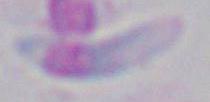
{
  "magnification": "1000x",
  "modality": "photomicrograph",
  "identification": "Toxoplasma gondii"
}